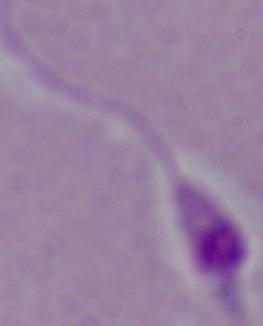

Summary:
  - Identification: Leishmania
  - Magnification: 1000x
  - Modality: photomicrograph